Point out each malaria parasite.
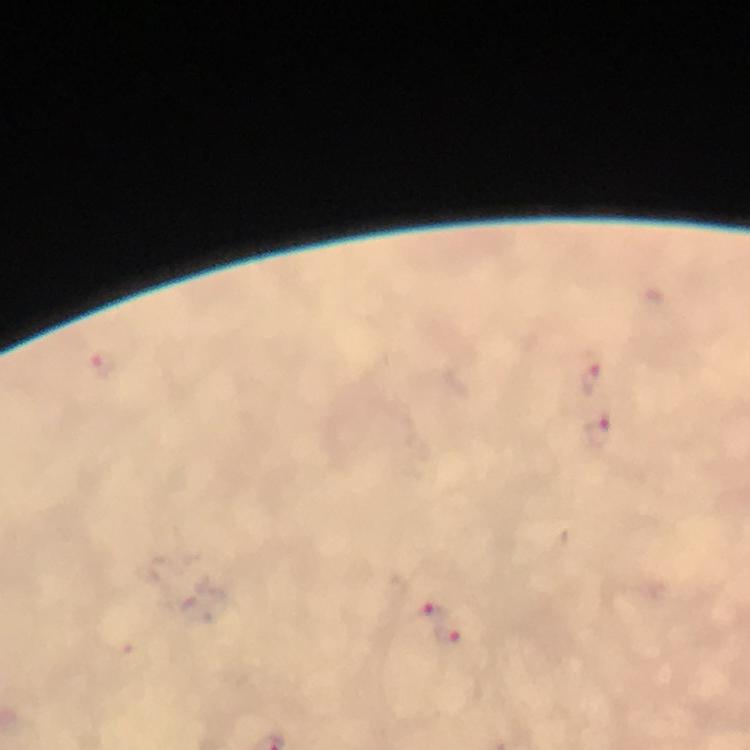
Approximate centers as (x, y) in pixels.
Malaria parasites: (101, 366), (592, 373), (601, 434), (429, 615), (448, 634).

{
  "magnification": "100x",
  "image_size": "750×750 pixels",
  "context": "from a malaria diagnostic workup",
  "cropped_from": "one field of view",
  "immersion_oil": "used",
  "preparation": "thick blood film",
  "capture": "smartphone mounted on the microscope",
  "stain": "Giemsa"
}